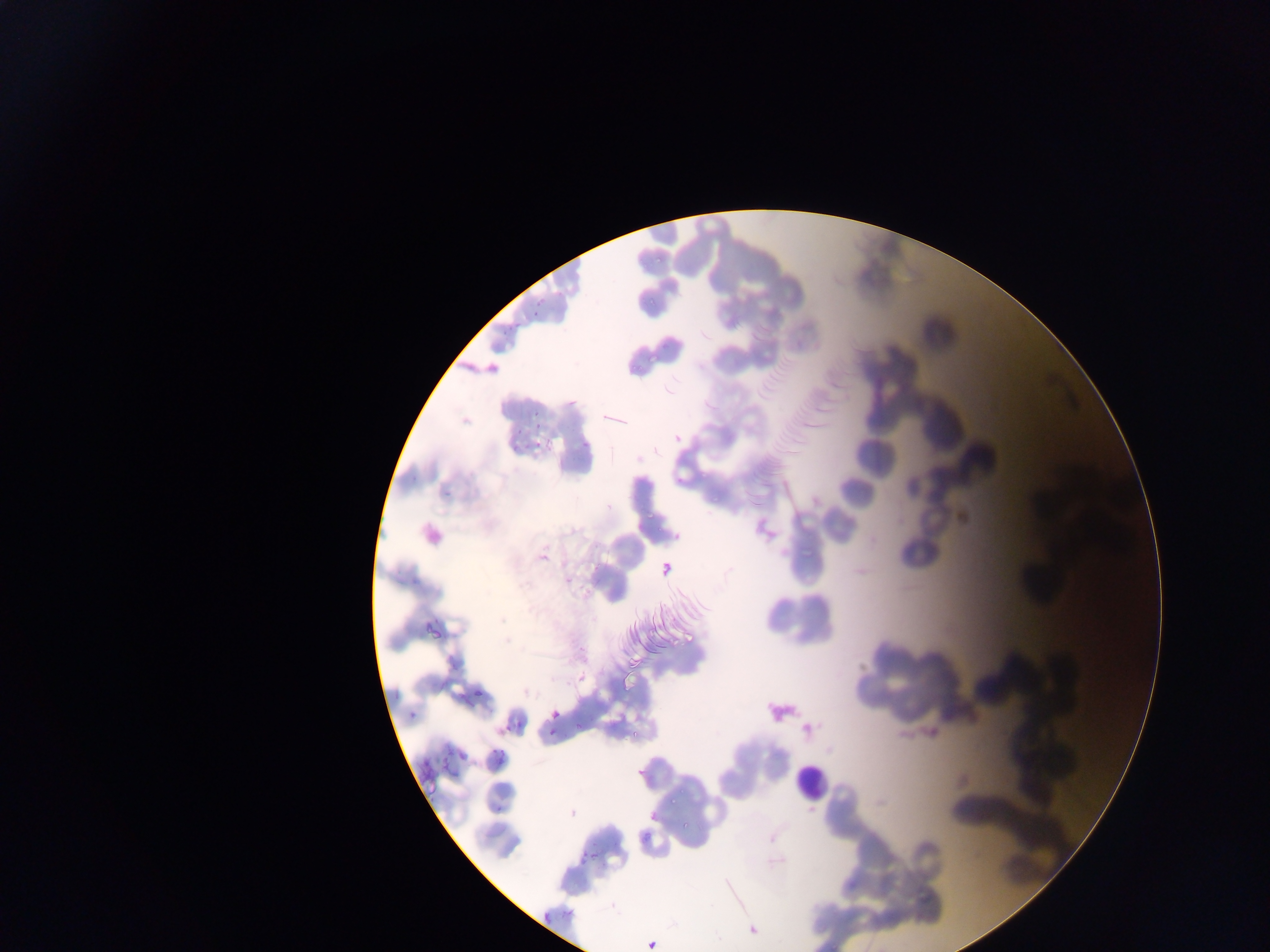
Approximate bounding boxes as (left, top, right, bottom) in pixels.
Summary:
  - Leukocyte locations: (793, 743, 825, 800)
  - Plasmodium parasite locations: (529, 280, 551, 314), (499, 319, 513, 332), (523, 404, 545, 427), (512, 419, 521, 435), (655, 560, 679, 583), (471, 689, 497, 697), (456, 693, 472, 709), (543, 702, 563, 725), (408, 707, 424, 719), (499, 708, 519, 730), (544, 724, 561, 737), (458, 744, 476, 757), (491, 748, 508, 768), (417, 750, 433, 764), (643, 806, 660, 827), (579, 836, 596, 867), (530, 900, 558, 921), (745, 922, 762, 940), (643, 933, 662, 952)
  - Field of view: single
  - Country: Ghana
  - Capture: mobile-phone photograph through a microscope
  - Image size: 1270×952 pixels
  - Preparation: thin blood film